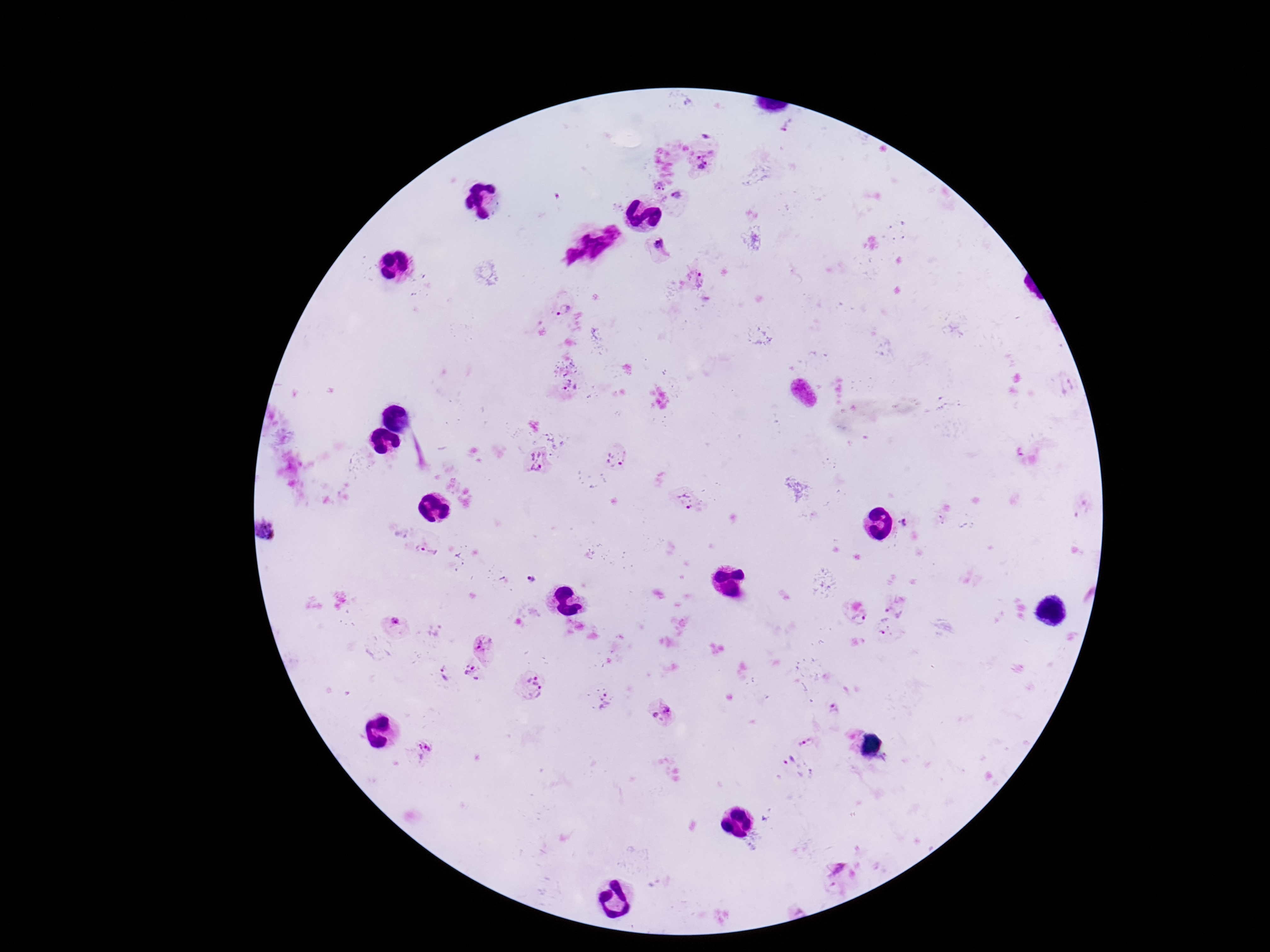
stain = Giemsa
Plasmodium parasite locations = approximate centers as {x, y} in pixels: {788, 125}, {707, 137}, {707, 161}, {660, 185}, {679, 195}, {659, 246}, {697, 278}, {565, 307}, {1071, 385}, {572, 388}, {1023, 453}, {618, 458}, {539, 463}, {692, 502}, {906, 523}, {271, 533}, {427, 551}, {534, 578}, {896, 603}, {859, 617}, {395, 620}, {880, 625}, {484, 643}, {472, 672}, {445, 674}, {533, 685}, {606, 701}, {834, 710}, {664, 714}, {805, 743}, {423, 751}, {786, 761}, {836, 869}
capture = smartphone camera through the microscope eyepiece
patient malaria status = infected
image size = 1270×952 pixels
field of view = one from this slide
magnification = 100x
preparation = thick blood smear